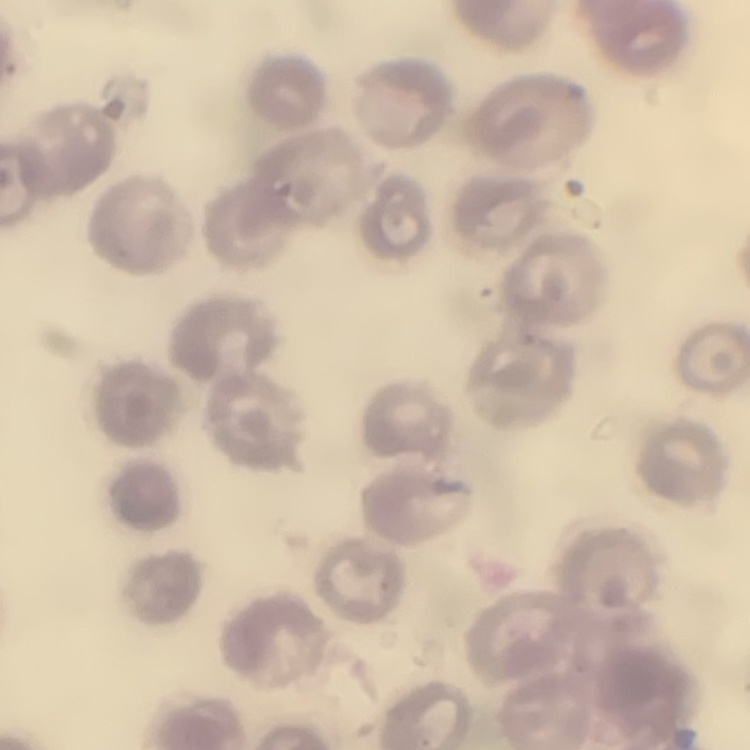

The erythrocytes exhibit no rouleaux formation. Field's or Giemsa stain. Thin blood smear. One tile cut from a larger photomicrograph.